Locate every Plasmodium parasite and every leukocyte.
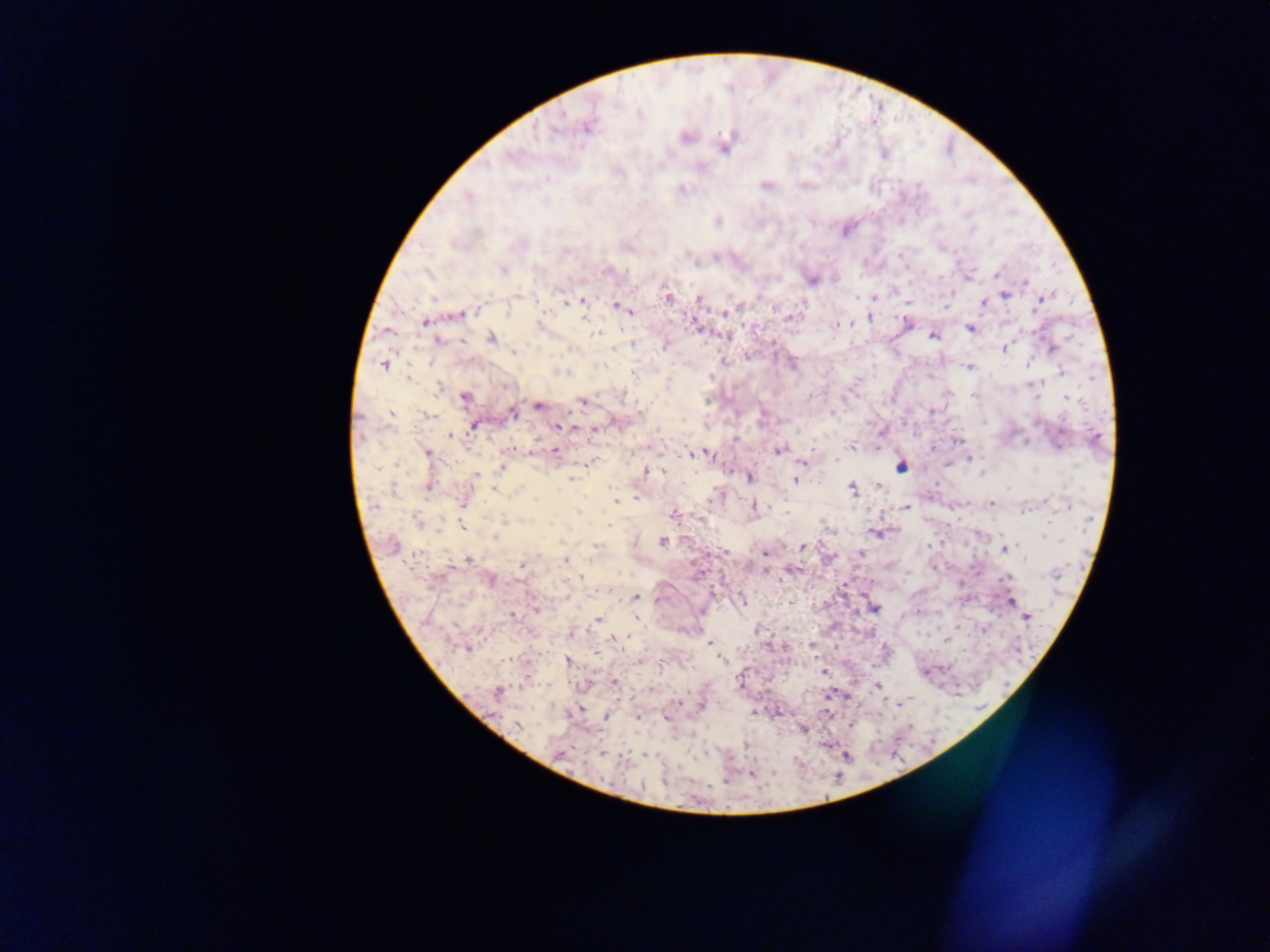

Approximate centers as [x, y] in pixels.
Plasmodium parasites: [639, 114], [584, 127], [686, 137], [723, 150], [547, 179], [765, 185], [681, 187], [717, 220], [691, 256], [693, 261], [504, 269], [996, 274], [812, 280], [1028, 280], [1026, 283], [1046, 295], [666, 296], [1005, 296], [874, 298], [583, 300], [699, 300], [983, 304], [565, 305], [613, 305], [626, 309], [1034, 309], [509, 311], [726, 311], [632, 312], [461, 314], [868, 317], [789, 318], [424, 322], [586, 322], [907, 322], [834, 325], [970, 329], [729, 335], [932, 336], [596, 337], [489, 338], [439, 340], [630, 344], [666, 346], [1003, 350], [515, 352], [383, 365], [970, 369], [1061, 372], [411, 376], [711, 377], [439, 387], [464, 398], [1068, 399], [583, 402], [536, 406], [512, 411], [932, 412], [392, 415], [429, 416], [558, 426], [474, 427], [576, 428], [594, 431], [448, 436], [851, 447], [932, 449], [779, 450], [554, 451], [425, 452], [701, 454], [693, 455], [969, 456], [804, 462], [950, 464], [502, 466], [900, 467], [645, 471], [664, 471], [476, 475], [749, 478], [569, 480], [794, 481], [428, 487], [851, 488], [611, 489], [517, 491], [636, 498], [463, 500], [616, 501], [990, 503], [907, 505], [754, 506], [579, 511], [672, 514], [416, 519], [608, 524], [462, 527], [497, 536], [1043, 537], [663, 540], [803, 546], [595, 547], [1004, 551], [765, 552], [417, 555], [564, 559], [469, 560], [520, 565], [791, 570], [580, 577], [1006, 577], [491, 579], [636, 598], [1011, 599], [533, 604], [536, 608], [511, 615], [636, 617], [1026, 617], [597, 620], [614, 639], [710, 643], [467, 648], [716, 650], [567, 661], [822, 672], [615, 681], [878, 686], [650, 688], [900, 700], [898, 702], [755, 712], [637, 718], [664, 718], [803, 729].
No leukocytes observed.

Mobile-phone photograph taken through the microscope. Collected in Ghana. Single field of view. Thick blood film. Image is 1270×952 pixels.